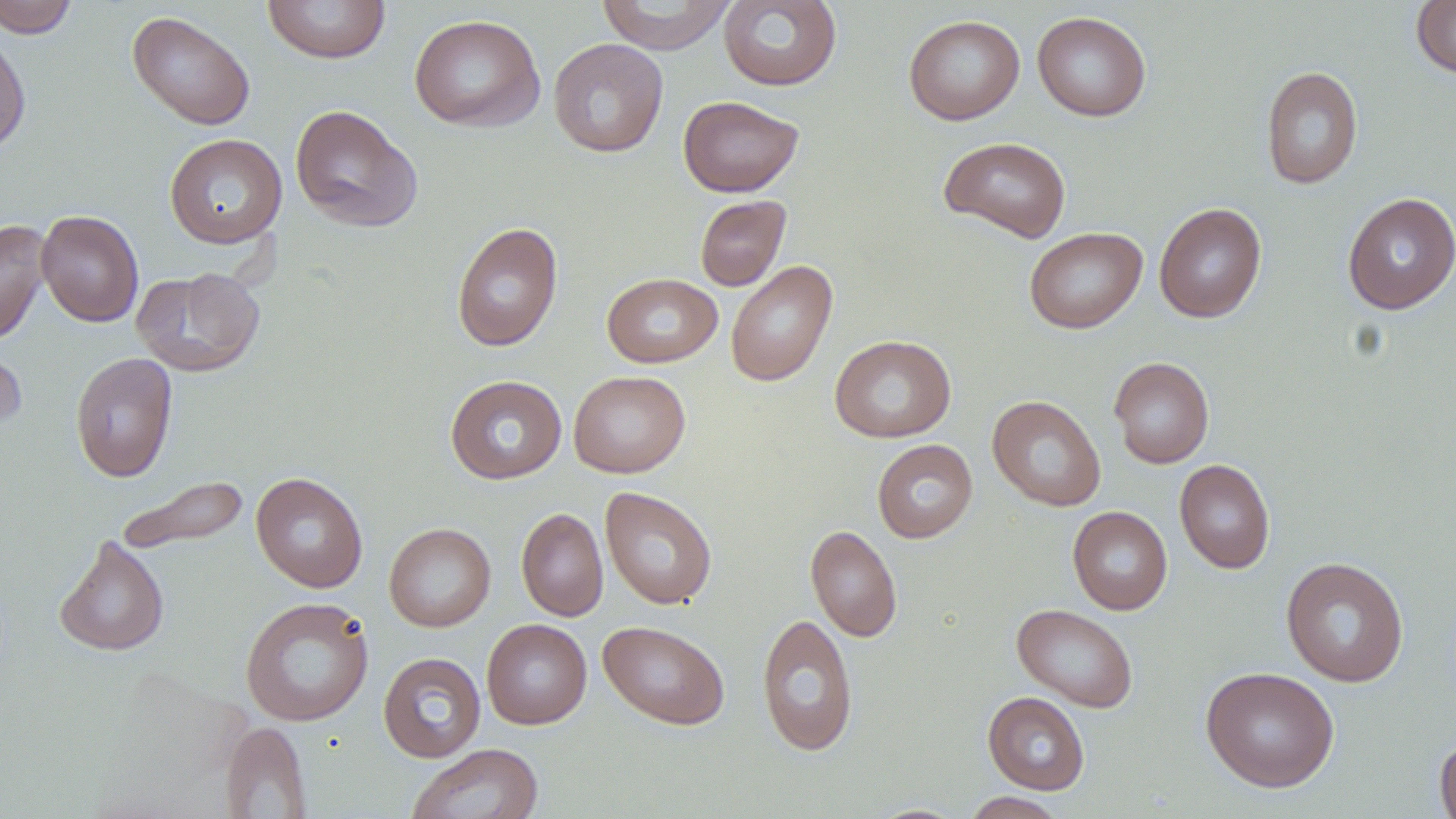

Approximate bounding boxes as (x1,y1)-(x2,y2) corner pairs in pixels. Uninfected red blood cell locations: (0,0)-(79,38), (595,0)-(736,54), (718,0)-(842,91), (262,1)-(391,64), (1411,1)-(1456,78), (127,10)-(255,130), (1032,11)-(1152,122), (408,14)-(546,132), (904,14)-(1025,125), (0,30)-(32,155), (548,38)-(668,158), (1260,65)-(1363,189), (677,95)-(804,198), (289,104)-(424,233), (164,133)-(287,249), (938,136)-(1071,243), (1342,192)-(1456,314), (695,195)-(791,291), (1154,202)-(1267,323), (36,209)-(143,327), (0,218)-(51,346), (450,222)-(563,352), (1024,226)-(1147,334), (725,260)-(838,387), (132,267)-(265,377), (602,272)-(723,368), (829,334)-(956,443), (0,336)-(27,438), (70,352)-(178,483), (1109,356)-(1214,469), (568,370)-(691,478), (445,374)-(567,484), (987,395)-(1105,512), (872,439)-(978,543), (1174,459)-(1275,574), (250,472)-(368,593), (116,475)-(249,556), (600,487)-(718,609), (1068,506)-(1173,615), (516,507)-(609,622), (383,522)-(496,632), (805,524)-(902,642), (54,535)-(169,657), (1281,556)-(1409,687), (240,596)-(374,727), (1012,603)-(1139,713), (756,612)-(858,757), (481,619)-(592,729), (598,620)-(731,730), (378,652)-(486,763), (1200,666)-(1340,792), (983,691)-(1090,794), (220,720)-(311,817), (1434,735)-(1456,819), (405,743)-(544,819), (962,791)-(1067,818), (865,803)-(971,818). Slide-level diagnosis: negative for blood parasites. Single field of view. May-Grünwald-Giemsa stain. Image is 1456×819 pixels. Light microscopy. Thin blood smear. 1000x magnification.